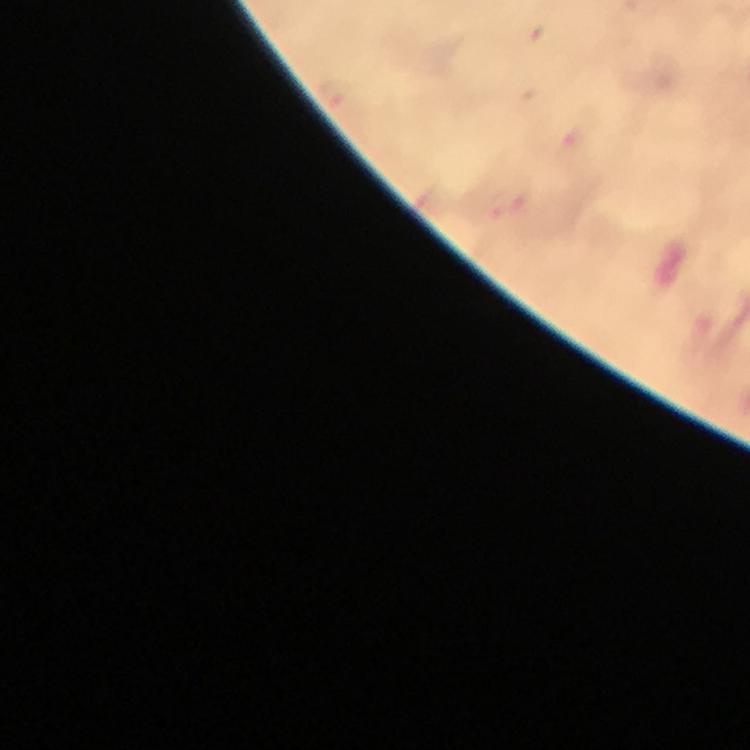
Approximate object centers, in pixels from the top-left corner.
Summary:
  - Malaria parasite locations: (x=334, y=95)
  - Cropped from: a single field of view
  - Stain: Giemsa
  - Immersion oil: applied
  - Magnification: 100x
  - Context: from a diagnostic examination for malaria
  - Preparation: thick blood smear
  - Image size: 750×750 pixels
  - Capture: smartphone mounted on the microscope